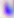
Photomicrograph. Captured at 400x magnification. Toxoplasma gondii is shown.